Point out each Plasmodium parasite.
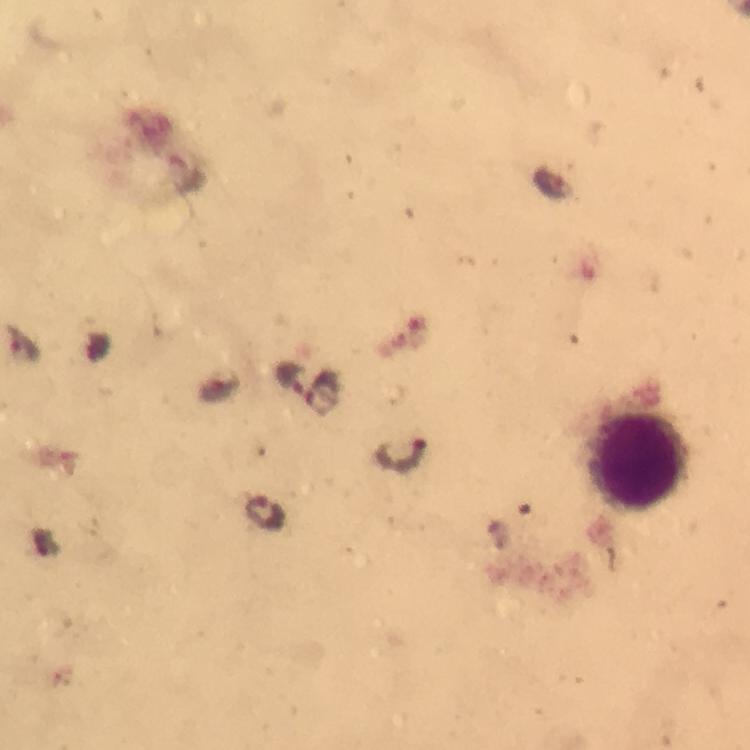
Approximate centers as [x, y] in pixels.
Plasmodium parasites: [290, 380], [323, 390], [402, 456], [266, 513].

Summary:
  - Leukocyte locations: [639, 464]
  - Stain: Giemsa
  - Image size: 750×750 pixels
  - Context: from a diagnostic examination for malaria
  - Capture: smartphone camera through the microscope
  - Magnification: 100x
  - Immersion oil: applied
  - Preparation: thick blood smear
  - Cropped from: a single field of view